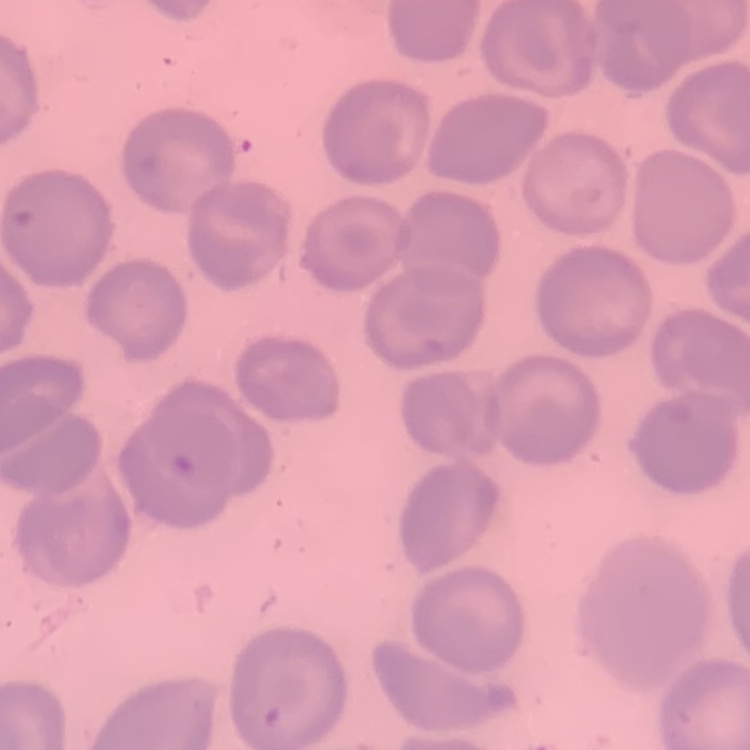
Summary:
  - Erythrocyte morphology: no rouleaux formation
  - Image type: square crop of a larger photomicrograph
  - Stain: Field's or Giemsa
  - Preparation: thin blood film